Identify the parasite.
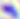

Toxoplasma gondii.

Photomicrograph. Captured at 400x magnification.